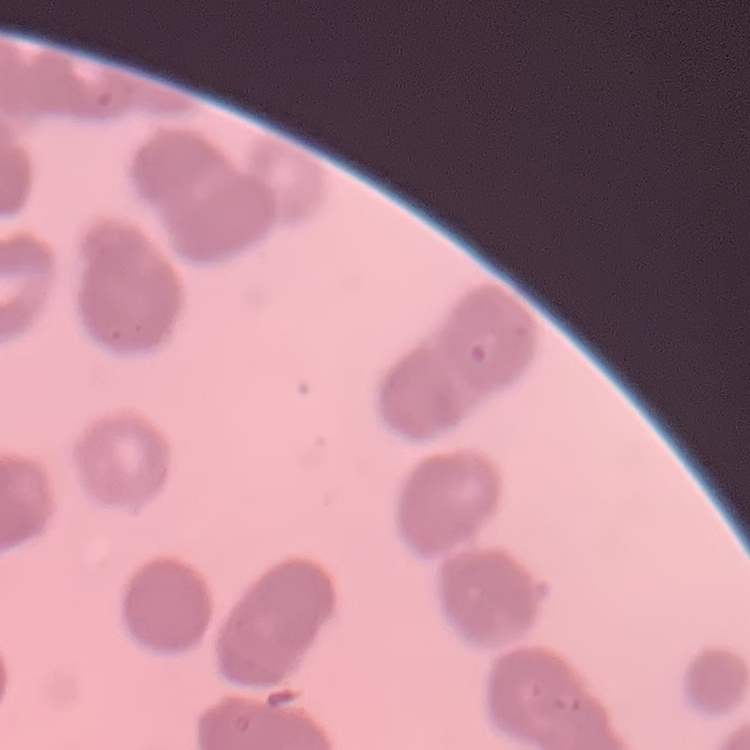

erythrocyte morphology = rouleaux formation
preparation = thin blood film
image type = one tile cut from a larger photomicrograph
stain = Field's or Giemsa